Assess the morphology of the red blood cells.
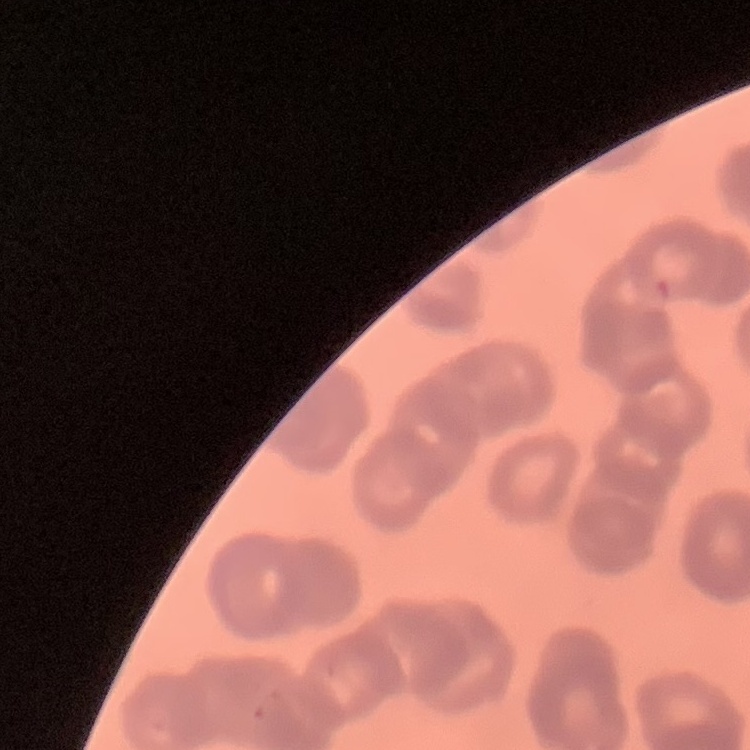
They show rouleaux formation.

Summary:
  - Preparation: thin blood film
  - Image type: one tile cut from a larger photomicrograph
  - Stain: Field's or Giemsa